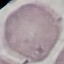
Malaria status: uninfected. Photographed with a smartphone camera at the microscope eyepiece. Thin smear of blood. Cell patch, automatically extracted from a larger field of view and resized to 64 × 64 pixels. Giemsa-stained preparation.